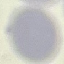

malaria status = uninfected
image type = cell patch, automatically extracted from a larger field of view and resized to 64 × 64 pixels
capture = smartphone camera at the microscope eyepiece
preparation = thin blood film
stain = Giemsa